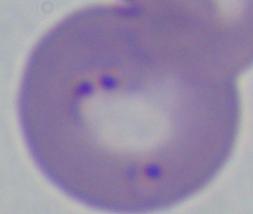
Photomicrograph. A Babesia parasite is seen. Captured at 1000x magnification.